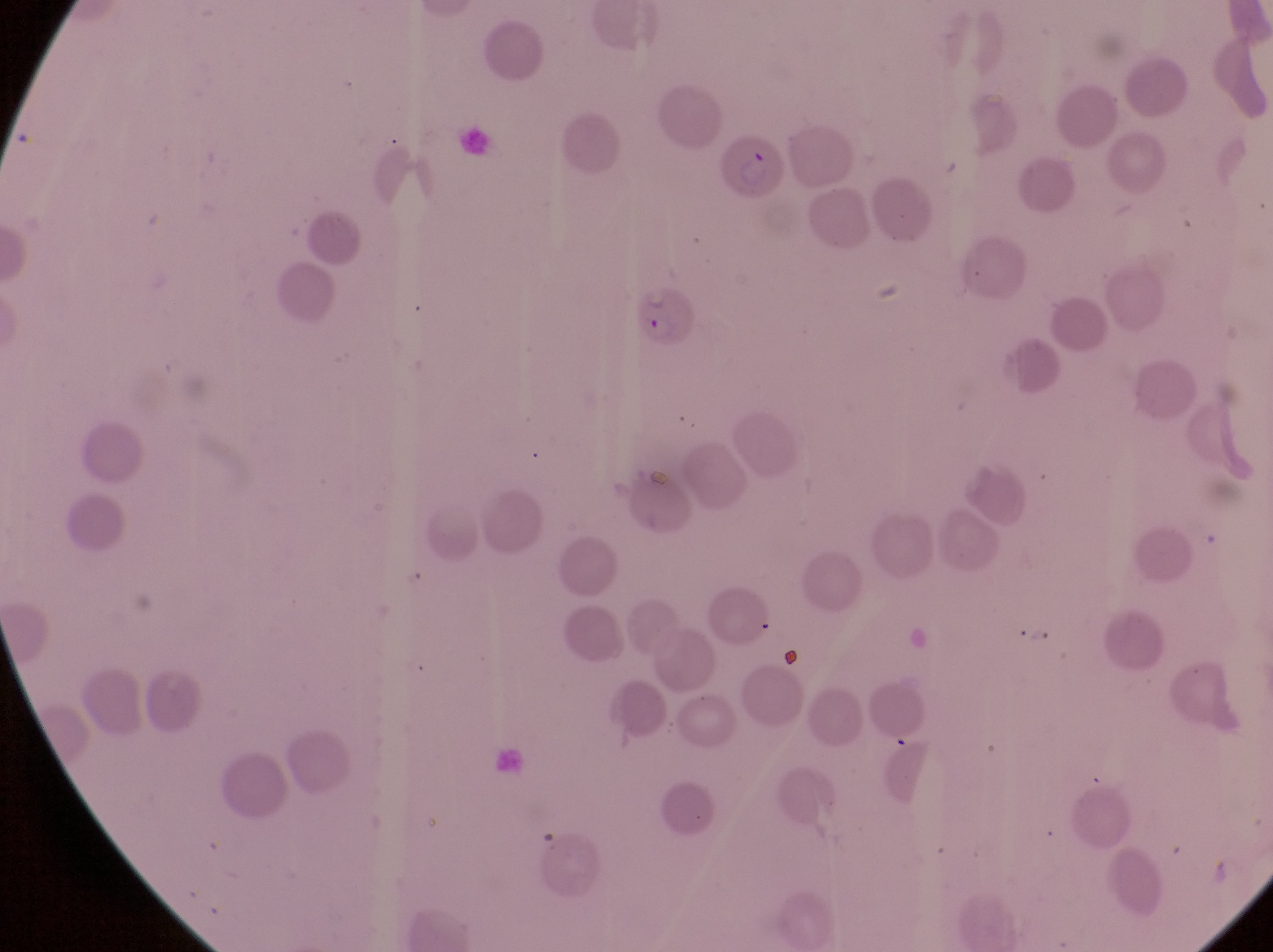
Approximate bounding boxes as {left, top, right, bottom} in pixels. Parasitised red blood cell locations: {719, 127, 788, 209}, {636, 287, 703, 355}. Magnification of 1000x. Image is 1273×952 pixels. Photographed through the eyepiece of an Olympus CX-23 microscope with a smartphone camera. Thin blood smear. One field of view. Collected in Uganda.